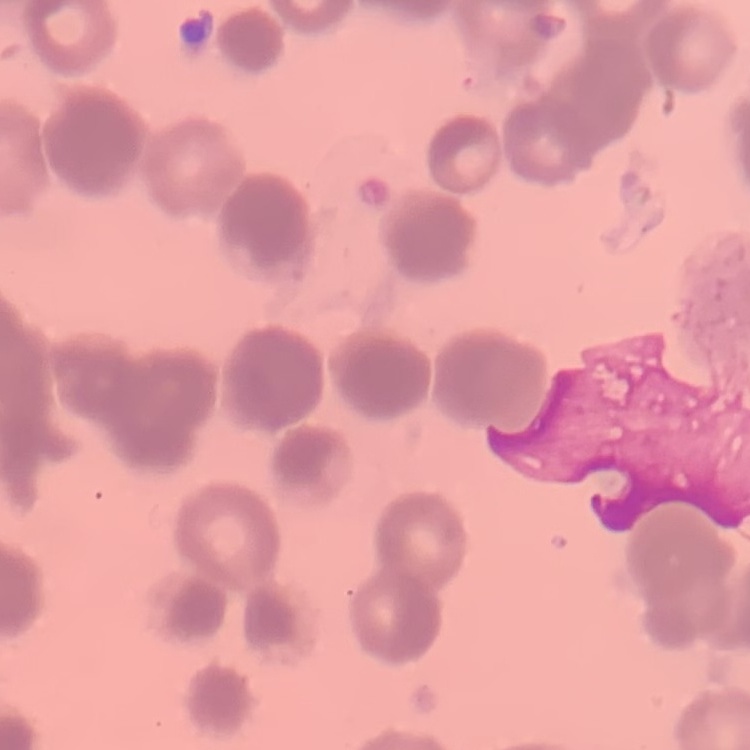
The red blood cells exhibit rouleaux formation. Field's or Giemsa stain. One tile cut from a larger photomicrograph. Thin peripheral smear.